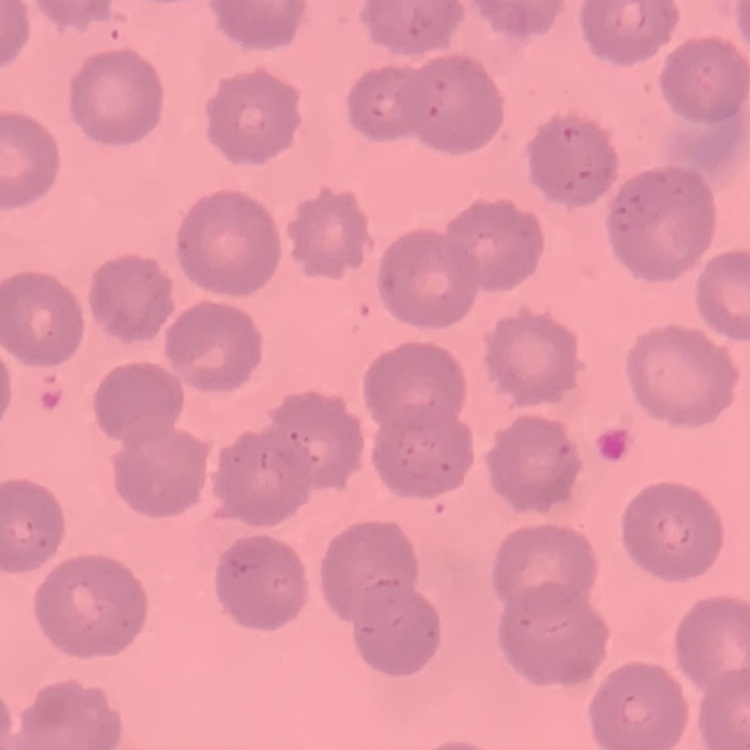
Summary:
  - Erythrocyte morphology: no rouleaux formation
  - Image type: one tile cut from a larger photomicrograph
  - Stain: Field's or Giemsa
  - Preparation: thin blood film